Report the malaria status of this cell.
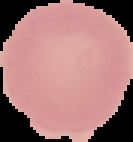
It is uninfected.

From a thin blood smear. Image is 133×142 pixels. The area outside the segmented cell region is set to black.